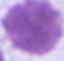
Captured at 1000x magnification. An erythrocyte is shown. Micrograph.